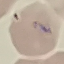 Malaria status: uninfected. Acquired by smartphone through the microscope eyepiece. Cell patch, automatically extracted from a larger field of view and resized to 64 × 64 pixels. Thin blood film. Giemsa stain.